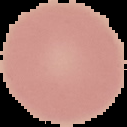
The area outside the segmented cell region is set to black. Result: negative for Plasmodium parasites. Image is 127×127 pixels. From a thin blood film.